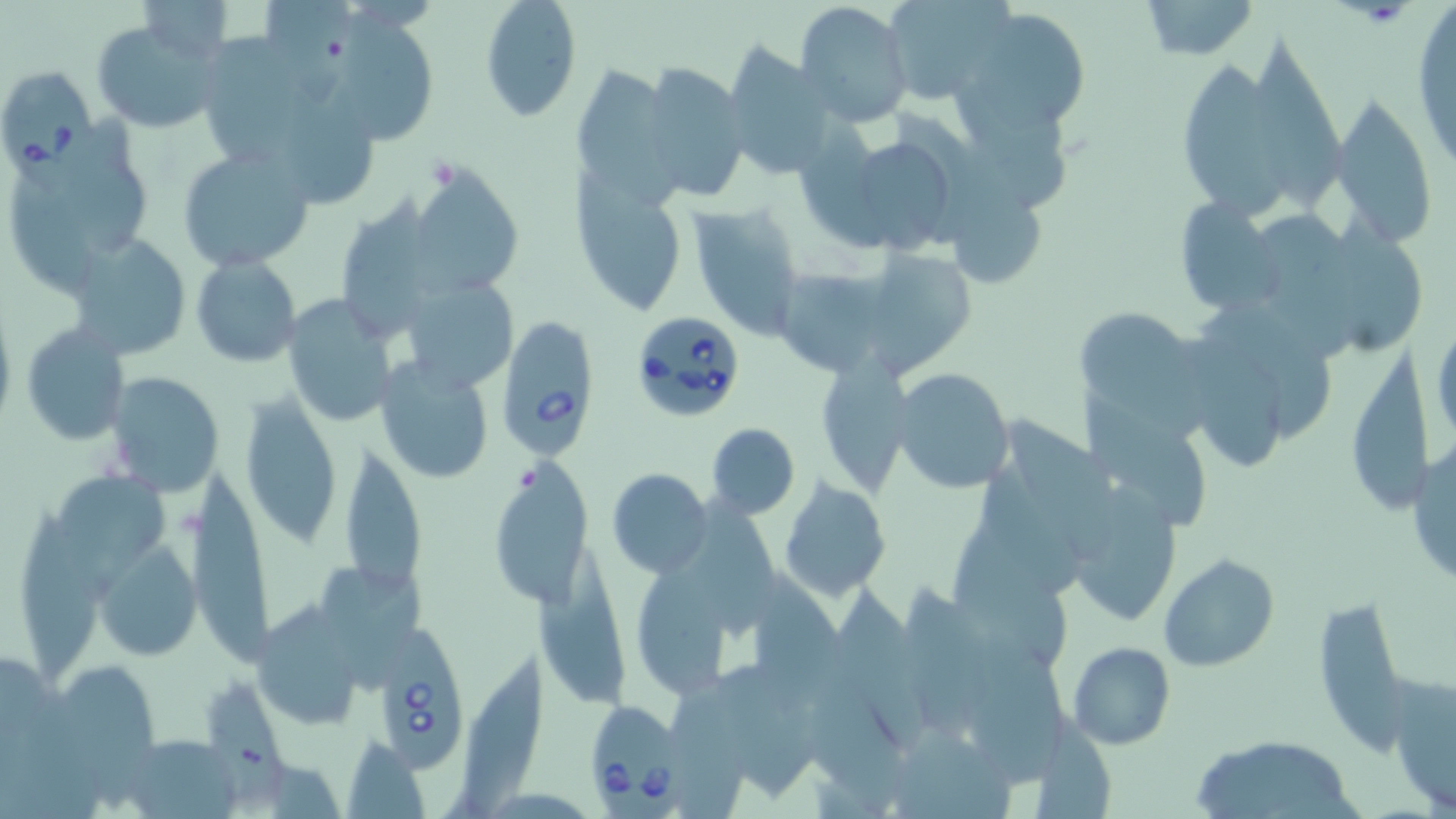 Approximate bounding boxes as [x1, y1, x2, y2] in pixels. Babesia divergens-infected red blood cell locations: [0, 63, 101, 201], [626, 310, 749, 423], [499, 315, 598, 454], [369, 629, 471, 771], [588, 697, 692, 819]. Uninfected red blood cell locations: [262, 0, 360, 107], [882, 0, 1009, 103], [1135, 0, 1260, 60], [136, 1, 233, 64], [479, 1, 581, 122], [795, 1, 914, 128], [959, 6, 1092, 134], [1409, 7, 1456, 172], [328, 11, 447, 143], [90, 15, 224, 133], [204, 29, 304, 162], [1245, 37, 1343, 219], [723, 42, 835, 181], [1183, 59, 1276, 222], [636, 60, 752, 202], [569, 63, 679, 197], [285, 76, 379, 204], [1330, 93, 1440, 249], [72, 113, 151, 255], [798, 119, 890, 253], [855, 142, 947, 251], [175, 144, 315, 272], [410, 161, 523, 299], [571, 172, 692, 315], [10, 173, 106, 292], [943, 177, 1051, 296], [341, 194, 432, 339], [1174, 197, 1281, 317], [683, 200, 804, 339], [1260, 208, 1355, 354], [1340, 215, 1421, 357], [69, 231, 194, 362], [870, 238, 974, 373], [190, 256, 302, 367], [772, 267, 889, 379], [407, 276, 515, 394], [282, 296, 399, 427], [1074, 302, 1212, 446], [1430, 309, 1455, 453], [1196, 310, 1333, 436], [21, 324, 131, 446], [1186, 342, 1284, 474], [1342, 342, 1437, 518], [815, 356, 915, 497], [375, 358, 495, 485], [892, 367, 1016, 494], [104, 370, 224, 498], [1082, 393, 1206, 530], [239, 394, 345, 549], [1008, 414, 1119, 565], [706, 422, 800, 519], [1406, 441, 1455, 591], [348, 448, 427, 598], [495, 459, 591, 609], [58, 467, 169, 603], [607, 468, 712, 577], [193, 470, 274, 667], [984, 472, 1079, 592], [1059, 475, 1184, 628], [780, 480, 896, 604], [693, 492, 777, 637], [19, 501, 98, 684], [951, 516, 1068, 661], [95, 540, 201, 660], [538, 550, 626, 709], [1160, 555, 1279, 670], [320, 565, 426, 693], [636, 569, 728, 698], [758, 570, 847, 684], [829, 574, 918, 704], [902, 581, 993, 742], [1312, 592, 1409, 748], [249, 610, 367, 732], [963, 636, 1063, 788], [1067, 642, 1175, 750], [463, 649, 545, 819], [717, 660, 825, 800], [63, 666, 158, 810], [806, 672, 906, 812], [1388, 673, 1455, 814], [205, 681, 288, 801], [670, 684, 749, 819], [1036, 714, 1116, 819], [895, 727, 1014, 819], [119, 733, 239, 817], [1192, 734, 1361, 816], [343, 736, 429, 817]. Slide-level diagnosis: Babesia divergens. Thin blood film. Image is 1456×819 pixels. One field of a larger specimen. Optical microscopy. May-Grünwald-Giemsa-stained preparation. Captured at 1000x magnification.